Outline platelets.
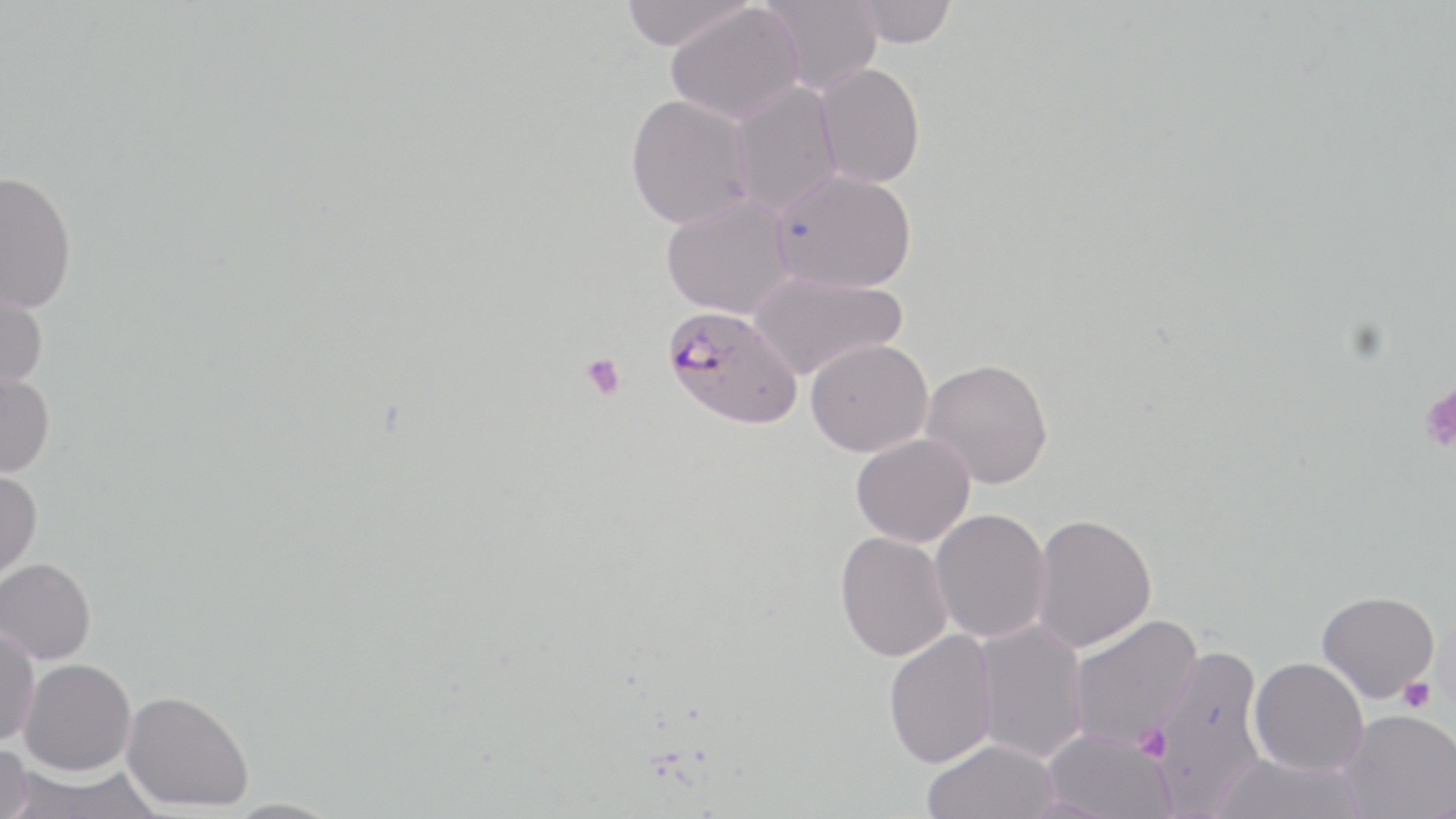
Approximate bounding boxes as [x1, y1, x2, y2] in pixels.
Platelets: [580, 352, 626, 400], [1418, 382, 1456, 453], [1397, 676, 1437, 712], [1134, 721, 1172, 762].

Plasmodium falciparum-infected red blood cell locations: [661, 305, 802, 430]. Uninfected red blood cell locations: [621, 0, 754, 51], [758, 0, 883, 96], [849, 1, 958, 47], [666, 4, 805, 125], [814, 63, 926, 188], [730, 82, 842, 217], [625, 94, 753, 230], [770, 168, 918, 294], [0, 171, 77, 313], [661, 195, 795, 319], [748, 271, 907, 380], [0, 278, 48, 392], [804, 338, 934, 457], [920, 358, 1053, 489], [0, 370, 55, 478], [851, 433, 975, 547], [0, 469, 43, 583], [929, 508, 1052, 643], [1030, 512, 1156, 653], [835, 531, 953, 662], [0, 558, 96, 664], [1317, 590, 1440, 703], [1067, 614, 1201, 750], [972, 619, 1088, 763], [0, 623, 40, 747], [883, 629, 998, 769], [1146, 643, 1268, 812], [1248, 657, 1369, 777], [18, 658, 136, 775], [120, 690, 253, 812], [1337, 709, 1456, 819], [1042, 728, 1177, 819], [921, 738, 1059, 819], [0, 741, 33, 819], [1210, 751, 1364, 818], [6, 763, 162, 819], [221, 799, 345, 819]. Slide-level diagnosis: Plasmodium falciparum. Optical microscopy. Thin blood film. One field of a larger specimen. May-Grünwald-Giemsa stain. 1000x magnification. Image is 1456×819 pixels.